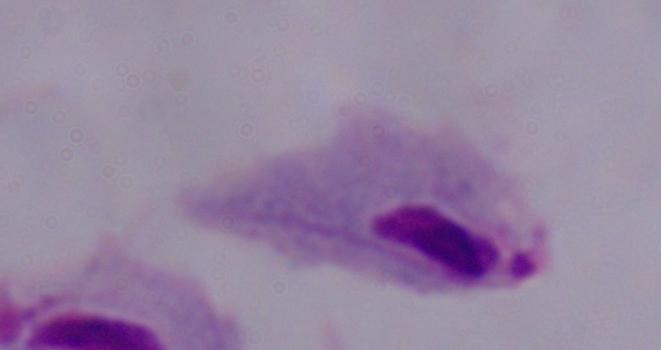

magnification = 1000x
modality = photomicrograph
identification = trichomonad